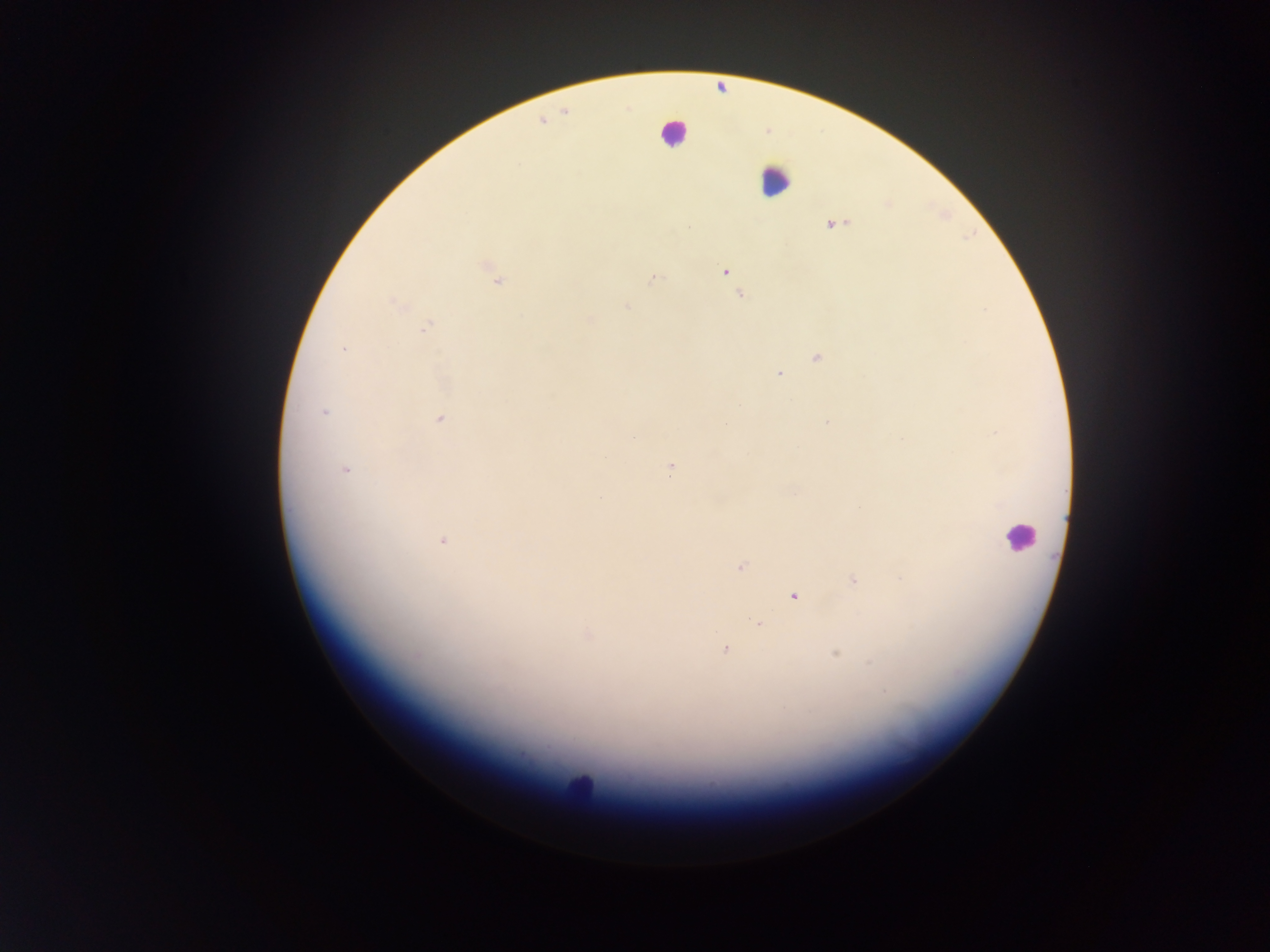

field of view = single
leukocyte locations = approximate centers as {x, y} in pixels: {673, 132}, {775, 180}, {1019, 535}, {576, 787}
capture = mobile-phone photograph through a microscope
malaria parasite locations = approximate centers as {x, y} in pixels: {833, 225}, {688, 227}, {724, 271}, {653, 279}, {498, 281}, {741, 295}, {395, 304}, {627, 307}, {986, 309}, {589, 319}, {426, 327}, {342, 349}, {816, 357}, {779, 374}, {324, 413}, {439, 420}, {827, 421}, {634, 437}, {346, 469}, {670, 470}, {443, 540}, {741, 566}, {901, 579}, {853, 580}, {793, 596}, {759, 624}, {588, 635}, {725, 650}, {836, 653}, {416, 656}, {871, 662}, {885, 691}
image size = 1270×952 pixels
preparation = thick blood film
country = Ghana